State which parasite is depicted.
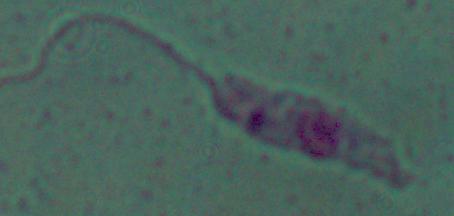
Leishmania.

{
  "modality": "photomicrograph",
  "magnification": "1000x"
}